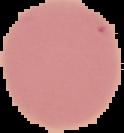
image type = cell region segmented out of the field of view; surrounding area masked to black
preparation = thin blood film
image size = 124×133 pixels
result = no Plasmodium parasites seen